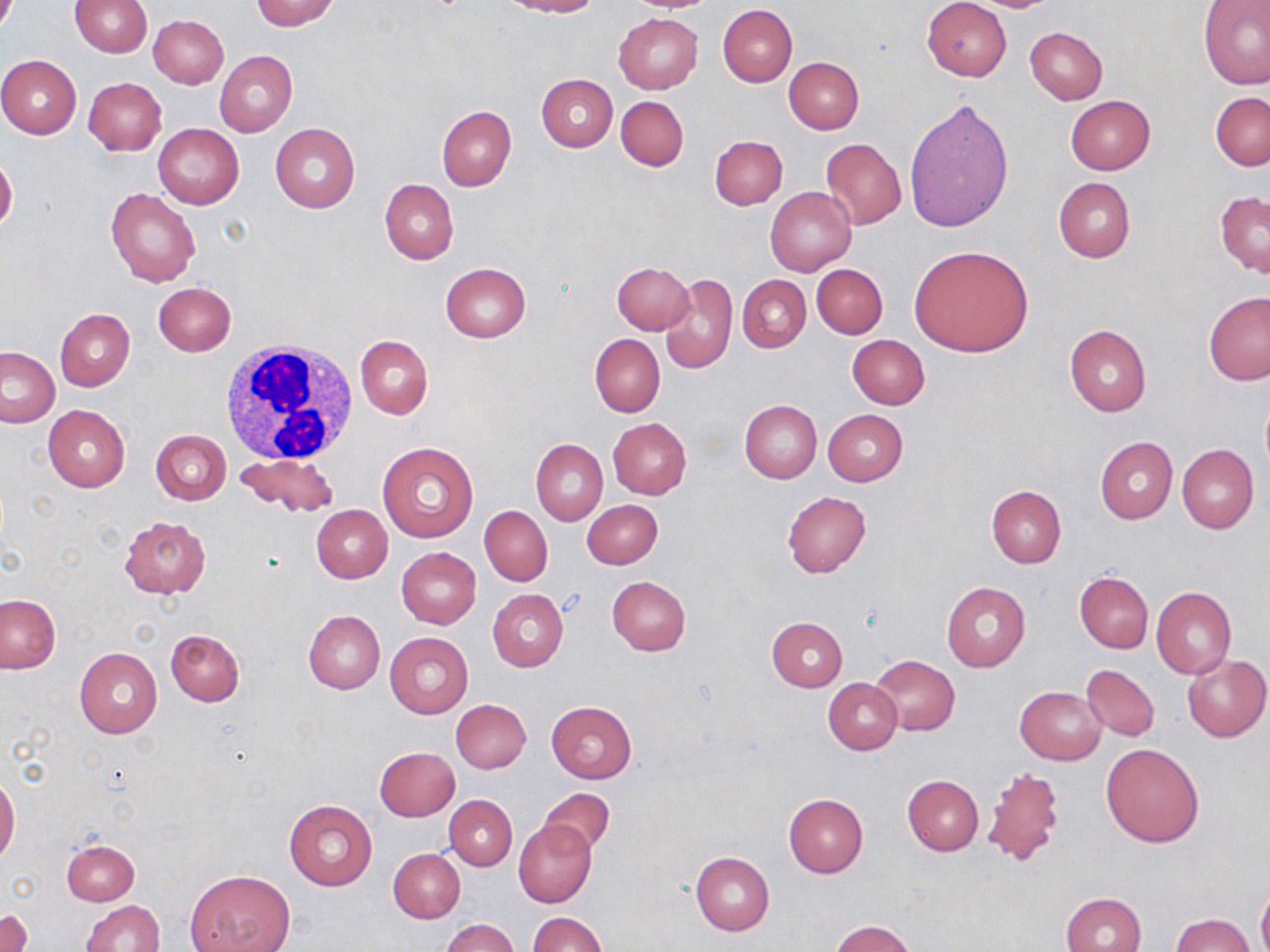

Summary:
  - Coordinate format: approximate bounding boxes as [x1, y1, x2, y2] in pixels
  - Uninfected red blood cell locations: [250, 0, 339, 29], [502, 0, 599, 17], [623, 0, 721, 13], [922, 0, 1012, 81], [70, 1, 152, 57], [1199, 1, 1270, 89], [718, 4, 797, 87], [614, 12, 703, 94], [149, 15, 228, 88], [1025, 26, 1108, 103], [215, 50, 297, 136], [0, 54, 81, 139], [783, 56, 863, 134], [536, 73, 617, 152], [83, 77, 166, 155], [1210, 91, 1269, 171], [1065, 95, 1155, 174], [616, 96, 688, 171], [904, 97, 1015, 233], [436, 106, 516, 190], [152, 122, 245, 209], [270, 123, 360, 213], [710, 135, 788, 210], [820, 138, 907, 230], [0, 155, 18, 232], [1053, 177, 1135, 263], [381, 179, 458, 264], [107, 187, 200, 287], [765, 187, 857, 277], [1215, 191, 1270, 277], [909, 245, 1035, 357], [612, 261, 693, 335], [441, 263, 531, 343], [811, 264, 887, 339], [661, 274, 738, 374], [737, 275, 810, 352], [153, 283, 235, 357], [1203, 291, 1270, 385], [54, 308, 135, 391], [1064, 325, 1151, 415], [354, 334, 432, 418], [590, 334, 665, 416], [847, 334, 930, 409], [1, 346, 60, 428], [1260, 396, 1270, 478], [739, 399, 821, 483], [43, 404, 129, 493], [822, 409, 907, 486], [608, 418, 692, 499], [150, 429, 231, 505], [1095, 436, 1177, 524], [530, 439, 607, 525], [377, 441, 478, 543], [1177, 445, 1258, 534], [235, 452, 338, 519], [987, 485, 1066, 568], [782, 492, 871, 577], [583, 500, 663, 569], [312, 505, 393, 583], [480, 505, 552, 586], [118, 516, 211, 598], [396, 547, 481, 629], [1074, 572, 1153, 653], [607, 576, 691, 655], [941, 582, 1031, 671], [1151, 587, 1236, 678], [488, 589, 568, 671], [1, 595, 60, 673], [304, 611, 385, 694], [766, 617, 846, 692], [165, 628, 244, 705], [384, 632, 474, 719], [74, 648, 162, 738], [1183, 654, 1270, 742], [870, 655, 960, 736], [1082, 664, 1158, 740], [824, 678, 902, 754], [1014, 686, 1105, 765], [451, 699, 531, 773], [546, 701, 636, 783], [1100, 743, 1204, 848], [374, 747, 459, 821], [981, 764, 1067, 868], [0, 774, 20, 864], [902, 774, 984, 855], [537, 789, 615, 856], [783, 794, 868, 877], [444, 795, 516, 870], [283, 799, 377, 891], [513, 819, 596, 907], [61, 838, 139, 906], [389, 848, 464, 922], [692, 851, 774, 935], [187, 869, 294, 952], [1256, 885, 1270, 952], [1060, 892, 1146, 952], [81, 899, 164, 952], [1, 909, 32, 952], [529, 912, 606, 952], [1171, 913, 1254, 951], [439, 917, 519, 952], [830, 920, 915, 952]
  - White blood cell locations: [216, 339, 364, 463]
  - Slide-level diagnosis: no evidence of blood parasites
  - Image size: 1270×952 pixels
  - Stain: May-Grünwald-Giemsa
  - Field of view: one of a larger specimen
  - Modality: light microscopy
  - Magnification: 1000x
  - Preparation: thin blood film